Locate leukocytes (white blood cells).
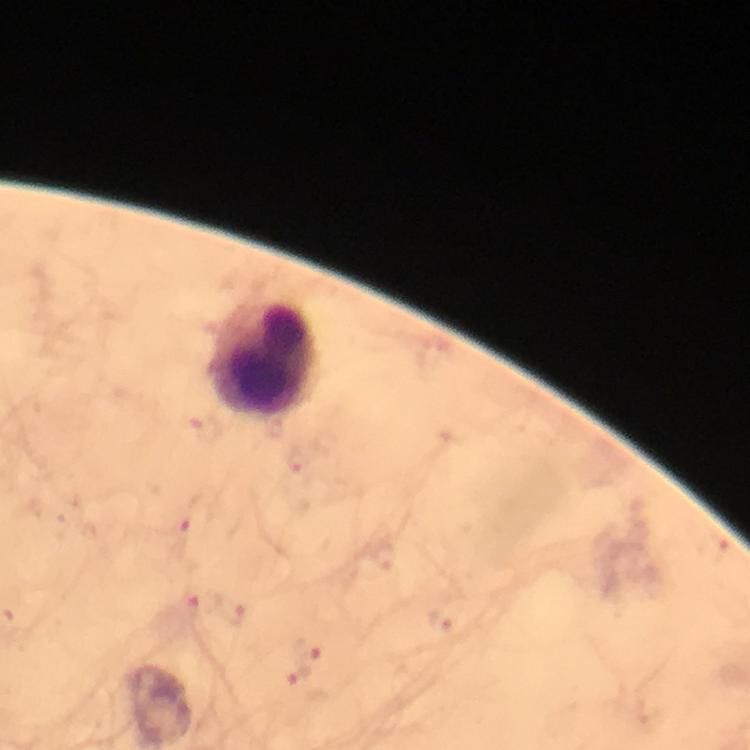
Approximate centers as [x, y] in pixels.
Leukocytes: [265, 358].

Plasmodium parasite locations: [206, 427], [296, 467], [196, 517], [713, 548], [196, 603], [234, 612], [442, 620], [308, 647], [300, 673]. Thick blood film. Photographed with a smartphone mounted on the microscope. 100x magnification. Giemsa stain. Image is 750×750 pixels. From a malaria diagnostic workup. Immersion oil applied. Cropped region of a single field of view.